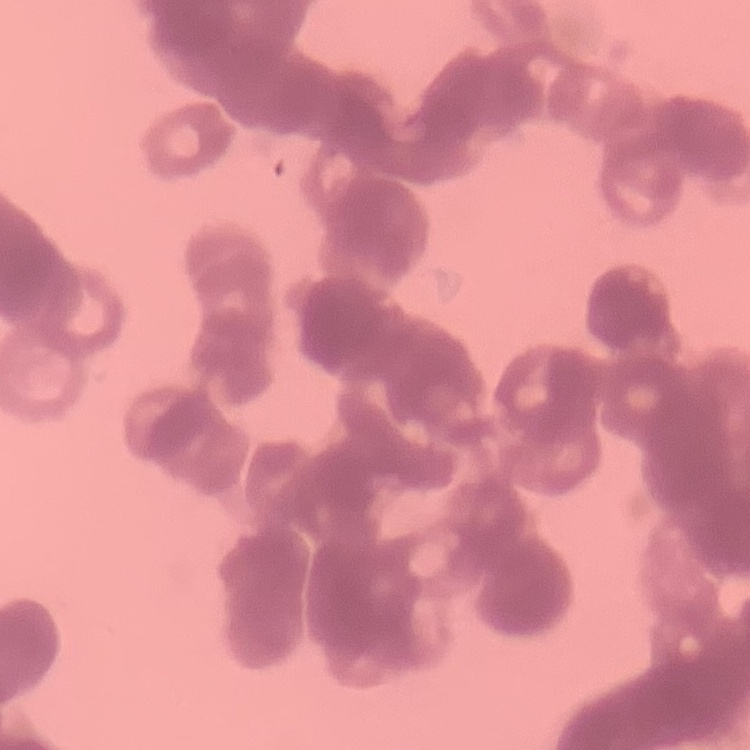

Summary:
  - Erythrocyte morphology: rouleaux formation
  - Stain: Field's or Giemsa
  - Preparation: thin blood film
  - Image type: square crop of a larger photomicrograph